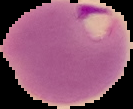

image size = 133×109 pixels
preparation = thin blood film
image type = segmented cell region with the area outside set to black
result = Plasmodium parasites identified